Locate and identify every blood parasite.
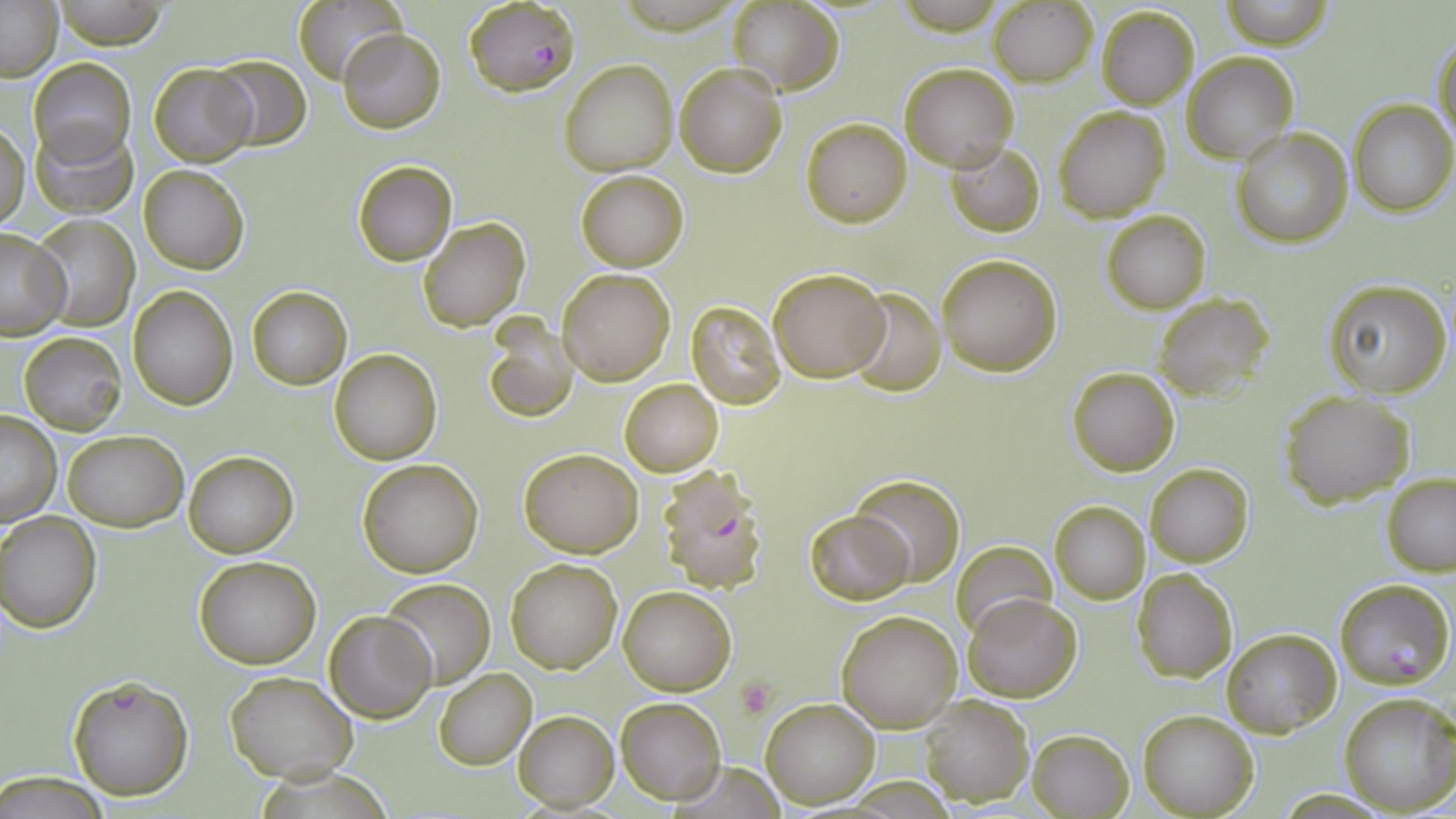

Approximate bounding boxes as [x1, y1, x2, y2] in pixels.
Plasmodium falciparum-infected red blood cells: [464, 0, 580, 97], [657, 469, 767, 591], [1334, 578, 1453, 690], [67, 675, 194, 802].
No Plasmodium ovale, Plasmodium malariae, Plasmodium vivax, Babesia divergens, or Trypanosoma brucei observed.

Summary:
  - Uninfected red blood cell locations: [53, 0, 168, 50], [0, 1, 62, 81], [293, 1, 404, 86], [725, 1, 845, 93], [1219, 1, 1334, 48], [988, 3, 1098, 86], [1096, 6, 1201, 110], [337, 27, 448, 133], [1432, 32, 1455, 148], [1183, 53, 1297, 164], [209, 54, 310, 150], [29, 58, 134, 165], [558, 58, 678, 175], [900, 62, 1018, 172], [674, 63, 787, 177], [149, 64, 256, 165], [1350, 99, 1455, 218], [1053, 105, 1173, 222], [801, 118, 911, 227], [29, 120, 139, 219], [1, 123, 28, 229], [1232, 129, 1353, 247], [946, 142, 1044, 236], [352, 161, 456, 265], [139, 165, 248, 274], [575, 170, 688, 271], [1101, 210, 1211, 313], [31, 215, 139, 331], [418, 217, 530, 332], [0, 229, 72, 339], [935, 253, 1062, 374], [769, 267, 891, 381], [556, 268, 675, 385], [1324, 279, 1452, 399], [129, 285, 236, 409], [246, 286, 352, 390], [841, 288, 945, 394], [1153, 292, 1270, 401], [686, 300, 785, 409], [483, 321, 580, 426], [19, 331, 127, 438], [330, 349, 443, 465], [1066, 366, 1180, 475], [620, 379, 724, 477], [1280, 390, 1414, 508], [0, 412, 61, 526], [62, 430, 188, 530], [518, 449, 642, 558], [184, 451, 298, 557], [356, 459, 484, 577], [1144, 463, 1253, 566], [851, 473, 965, 586], [1381, 473, 1456, 575], [1050, 501, 1149, 604], [805, 509, 913, 603], [0, 512, 102, 634], [951, 542, 1057, 641], [193, 556, 321, 669], [505, 558, 622, 673], [1132, 569, 1238, 684], [379, 577, 495, 690], [618, 585, 737, 695], [963, 593, 1082, 702], [836, 609, 965, 732], [325, 610, 437, 723], [1221, 629, 1340, 736], [434, 667, 536, 769], [225, 672, 355, 782], [1339, 692, 1456, 816], [919, 695, 1032, 805], [616, 696, 725, 804], [761, 698, 880, 808], [515, 710, 619, 810], [1138, 710, 1257, 817], [1027, 727, 1133, 819], [1, 773, 115, 817]
  - Platelet locations: [737, 678, 774, 719]
  - Slide-level diagnosis: Plasmodium falciparum
  - Stain: May-Grünwald-Giemsa
  - Preparation: thin blood film
  - Field of view: single
  - Image size: 1456×819 pixels
  - Magnification: 1000x
  - Modality: light microscopy